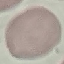

malaria_status: uninfected
stain: Giemsa
preparation: thin blood film
capture: smartphone camera at the microscope eyepiece
image_type: cell patch, automatically extracted from a larger field of view and resized to 64 × 64 pixels